Report the malaria status of this cell.
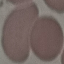
It is uninfected.

Thin blood film. Cell patch, automatically extracted from a larger field of view and resized to 64 × 64 pixels. Acquired by smartphone through the microscope eyepiece. Giemsa-stained preparation.